Locate every Plasmodium parasite and every leukocyte.
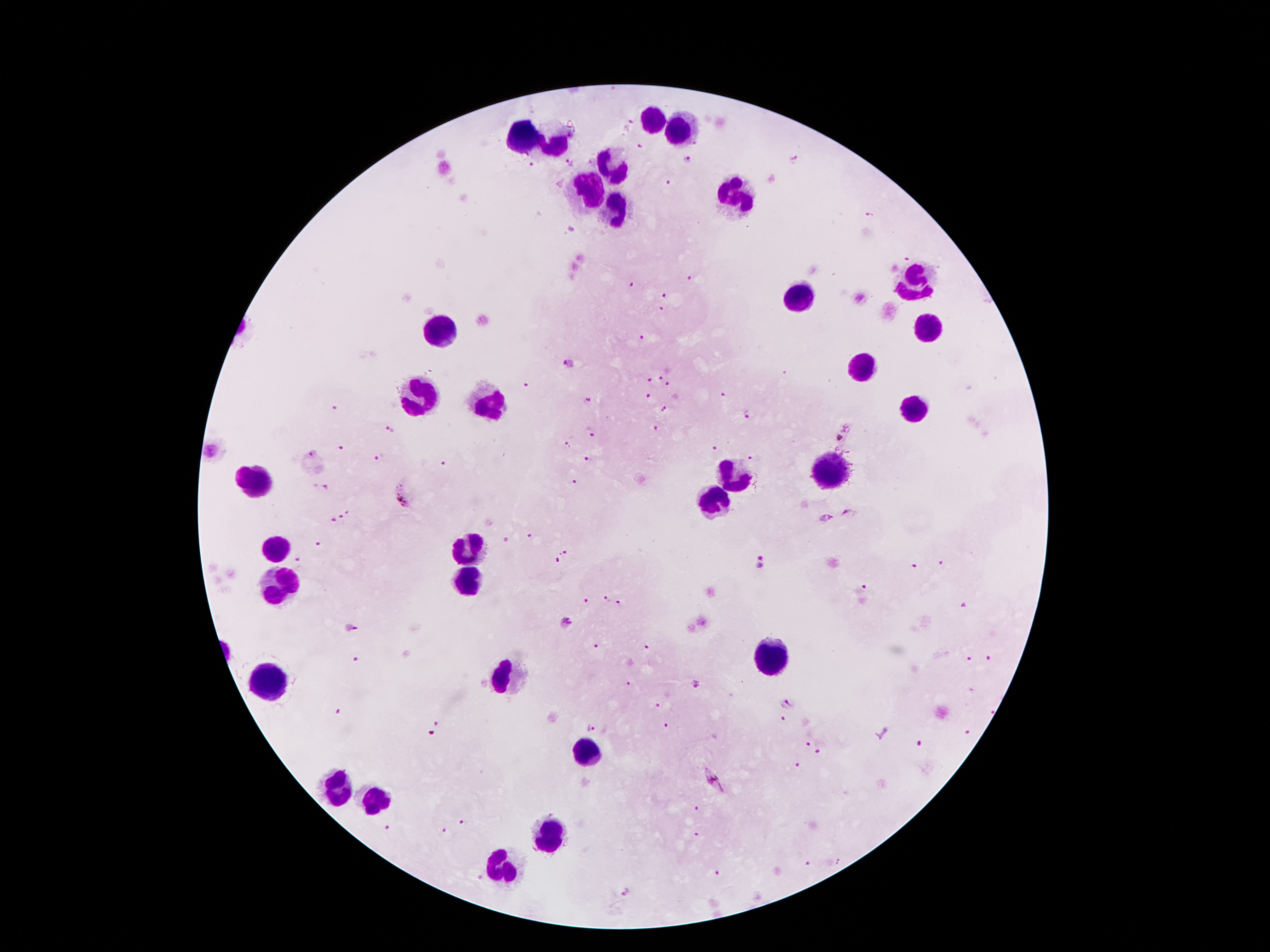
Approximate object centers, in pixels from the top-left corner.
Plasmodium parasites: (x=632, y=121), (x=640, y=143), (x=687, y=159), (x=795, y=161), (x=570, y=162), (x=530, y=165), (x=667, y=182), (x=868, y=215), (x=905, y=258), (x=690, y=278), (x=629, y=283), (x=665, y=296), (x=860, y=297), (x=662, y=309), (x=642, y=337), (x=570, y=365), (x=661, y=378), (x=648, y=379), (x=667, y=384), (x=523, y=385), (x=721, y=393), (x=648, y=397), (x=587, y=399), (x=338, y=409), (x=663, y=410), (x=749, y=415), (x=390, y=427), (x=656, y=428), (x=843, y=433), (x=592, y=435), (x=568, y=444), (x=715, y=447), (x=341, y=448), (x=313, y=453), (x=381, y=456), (x=752, y=457), (x=587, y=459), (x=444, y=464), (x=574, y=482), (x=405, y=495), (x=349, y=511), (x=846, y=512), (x=339, y=515), (x=823, y=519), (x=332, y=520), (x=530, y=536), (x=505, y=539), (x=319, y=544), (x=566, y=552), (x=557, y=559), (x=295, y=560), (x=761, y=562), (x=941, y=563), (x=914, y=566), (x=864, y=589), (x=608, y=599), (x=585, y=601), (x=620, y=604), (x=965, y=605), (x=565, y=622), (x=351, y=628), (x=597, y=647), (x=357, y=658), (x=986, y=658), (x=968, y=659), (x=694, y=682), (x=629, y=683), (x=656, y=702), (x=787, y=703), (x=337, y=712), (x=782, y=719), (x=438, y=724), (x=666, y=724), (x=591, y=730), (x=964, y=731), (x=805, y=740), (x=919, y=743), (x=818, y=750), (x=796, y=763), (x=716, y=781), (x=697, y=807), (x=463, y=822), (x=388, y=829), (x=441, y=832), (x=696, y=834), (x=808, y=863), (x=716, y=871), (x=624, y=894).
Leukocytes: (x=652, y=118), (x=681, y=130), (x=524, y=136), (x=556, y=145), (x=608, y=164), (x=590, y=193), (x=733, y=196), (x=617, y=209), (x=913, y=279), (x=795, y=298), (x=926, y=325), (x=441, y=330), (x=865, y=364), (x=418, y=400), (x=490, y=404), (x=913, y=407), (x=827, y=468), (x=734, y=472), (x=257, y=482), (x=713, y=495), (x=279, y=545), (x=465, y=547), (x=466, y=580), (x=281, y=588), (x=768, y=659), (x=506, y=677), (x=266, y=682), (x=586, y=752), (x=336, y=784), (x=375, y=793), (x=550, y=834), (x=500, y=868).

Thick blood smear. 100x magnification. Smartphone photograph taken through the microscope eyepiece. Giemsa-stained preparation. One field from this slide. Patient malaria status: infected with Plasmodium falciparum. Image is 1270×952 pixels.